Name the parasite shown.
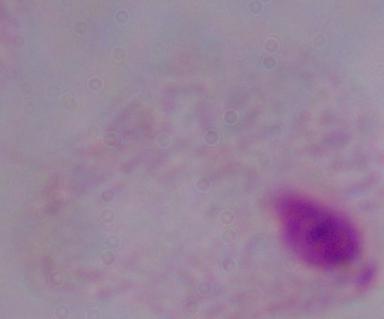
A trichomonad.

1000x magnification. Photomicrograph.